Locate every leukocyte (white blood cell).
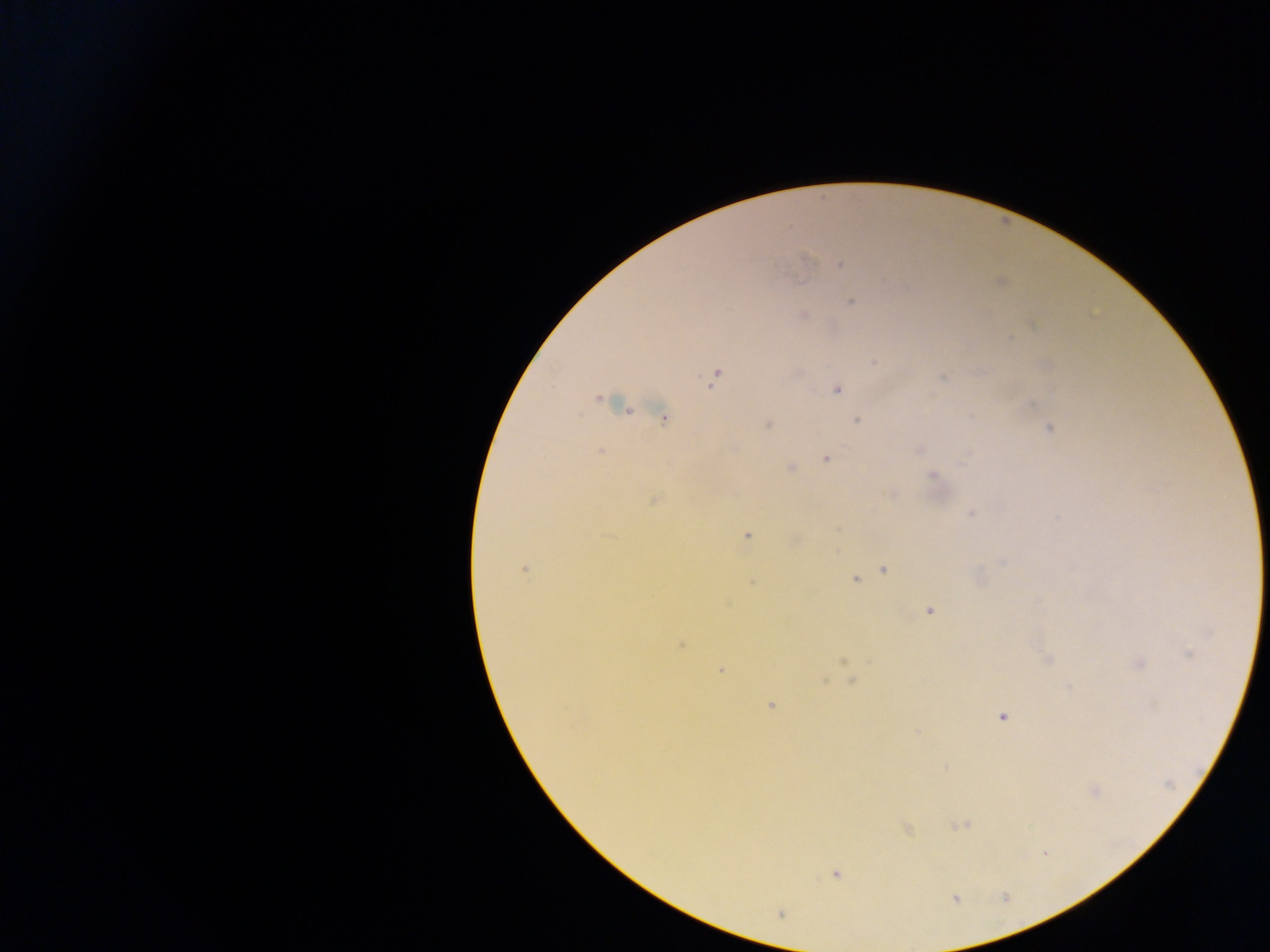

No leukocytes observed.

field_of_view: single
plasmodium_parasite_locations: 'approximate centers as [x, y] in pixels: [807, 258], [841, 265], [852, 302], [803, 316], [873, 363], [715, 377], [837, 389], [599, 399], [664, 418], [857, 421], [768, 426], [1049, 429], [601, 450], [918, 450], [826, 459], [790, 468], [933, 475], [891, 494], [654, 501], [971, 514], [747, 535], [1003, 563], [524, 569], [885, 570], [855, 580], [752, 582], [930, 611], [681, 644], [1189, 653], [1048, 659], [843, 661], [1139, 663], [720, 670], [852, 681], [770, 706], [1003, 717], [917, 731], [1094, 790], [960, 825], [907, 828], [1045, 853], [836, 874], [780, 913]'
country: Ghana
image_size: 1270×952 pixels
capture: mobile-phone photograph through a microscope
preparation: thick blood smear